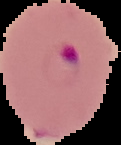

Summary:
  - Preparation: thin blood film
  - Malaria status: parasitized
  - Image size: 121×145 pixels
  - Image type: cell region segmented out of the field of view; surrounding area masked to black